Name the parasite shown.
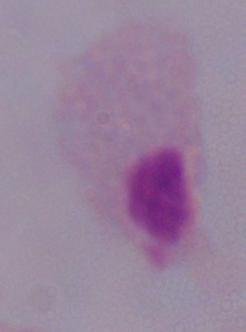
This is a trichomonad.

{
  "magnification": "1000x",
  "modality": "micrograph"
}